Assess the morphology of the erythrocytes.
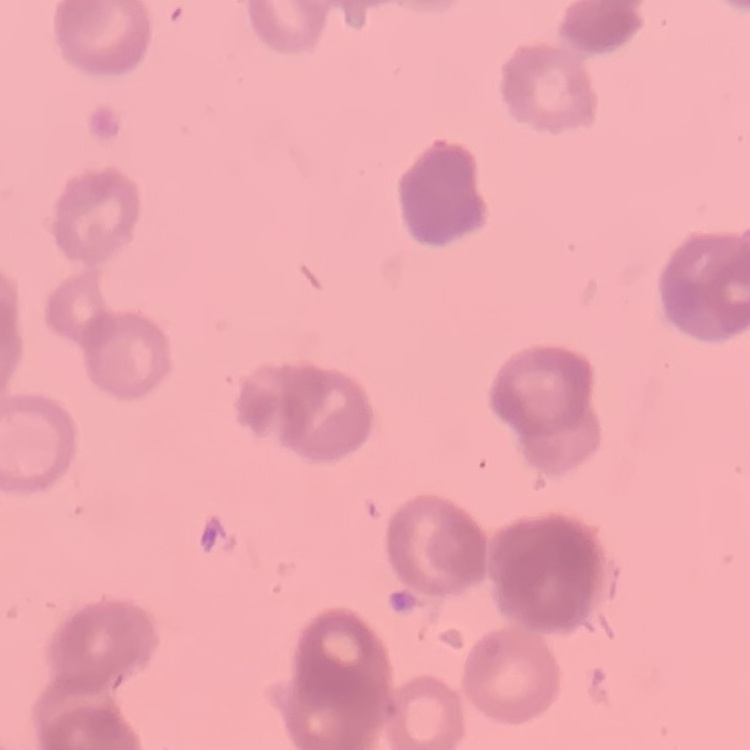
They show rouleaux formation.

One tile cut from a larger photomicrograph. Stained with either Field's or Giemsa. Thin peripheral smear.